Outline each P. falciparum parasite and classify it by life-cycle stage.
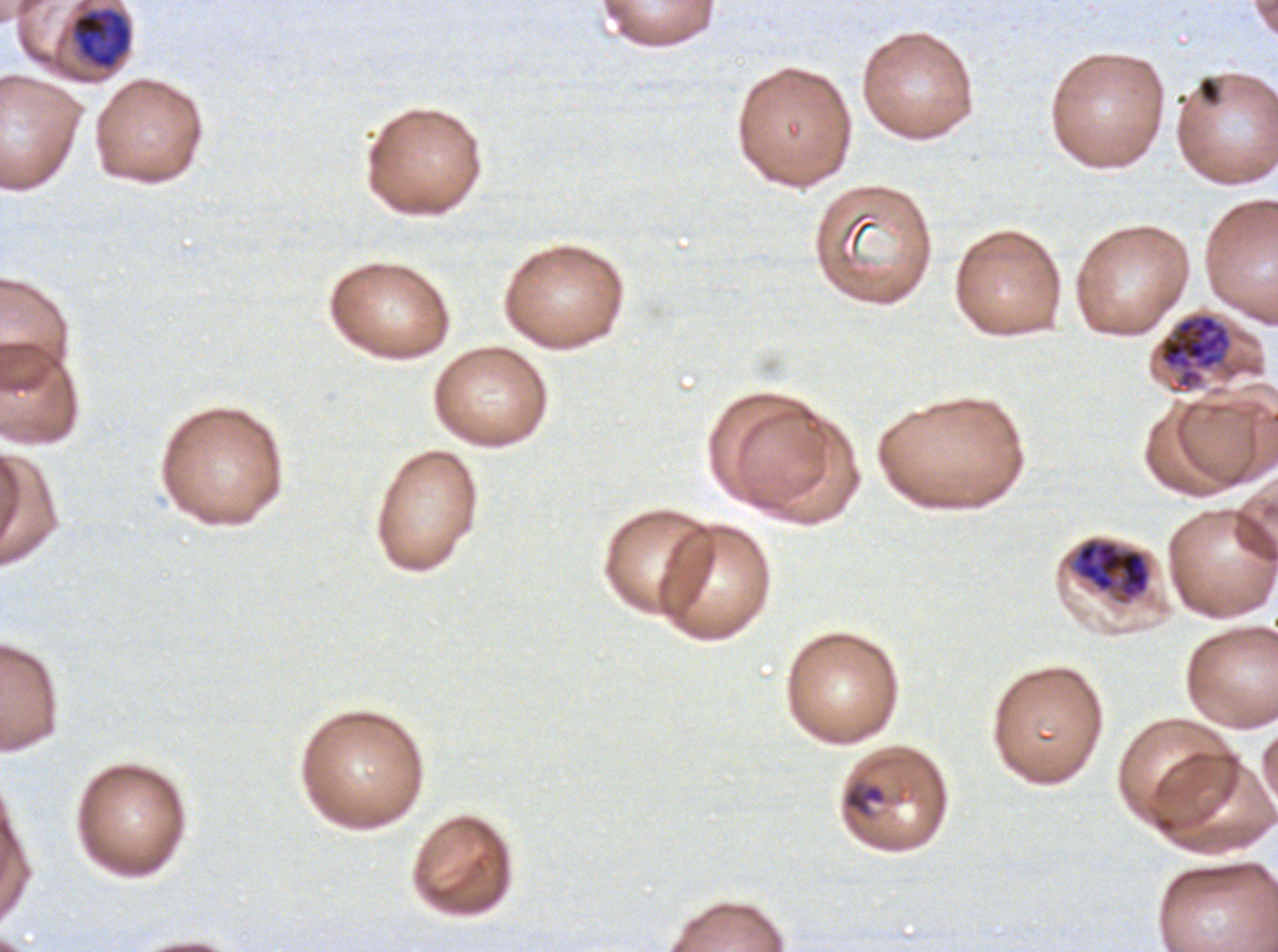
Approximate bounding rectangles given as corner coordinates in pixels from the top-left.
Rings: (x1=843, y1=779, x2=887, y2=818).
Late trophozoites: (x1=71, y1=7, x2=132, y2=69).
Late schizonts: (x1=1157, y1=312, x2=1234, y2=392), (x1=1070, y1=536, x2=1152, y2=605).
No late-ring/early-trophozoite forms, mid trophozoites, early schizonts, segmenters, or gametocytes observed.

debris locations = (x1=1198, y1=76, x2=1222, y2=106)
image size = 1278×952 pixels
preparation = thin blood smear
field of view = one sub-image of a larger composite
specimen = P. falciparum from a patient in The Gambia, cultured ex vivo for 24 to 48 hours
life-cycle stages observed = ring, late trophozoite, late schizont
stain = Giemsa